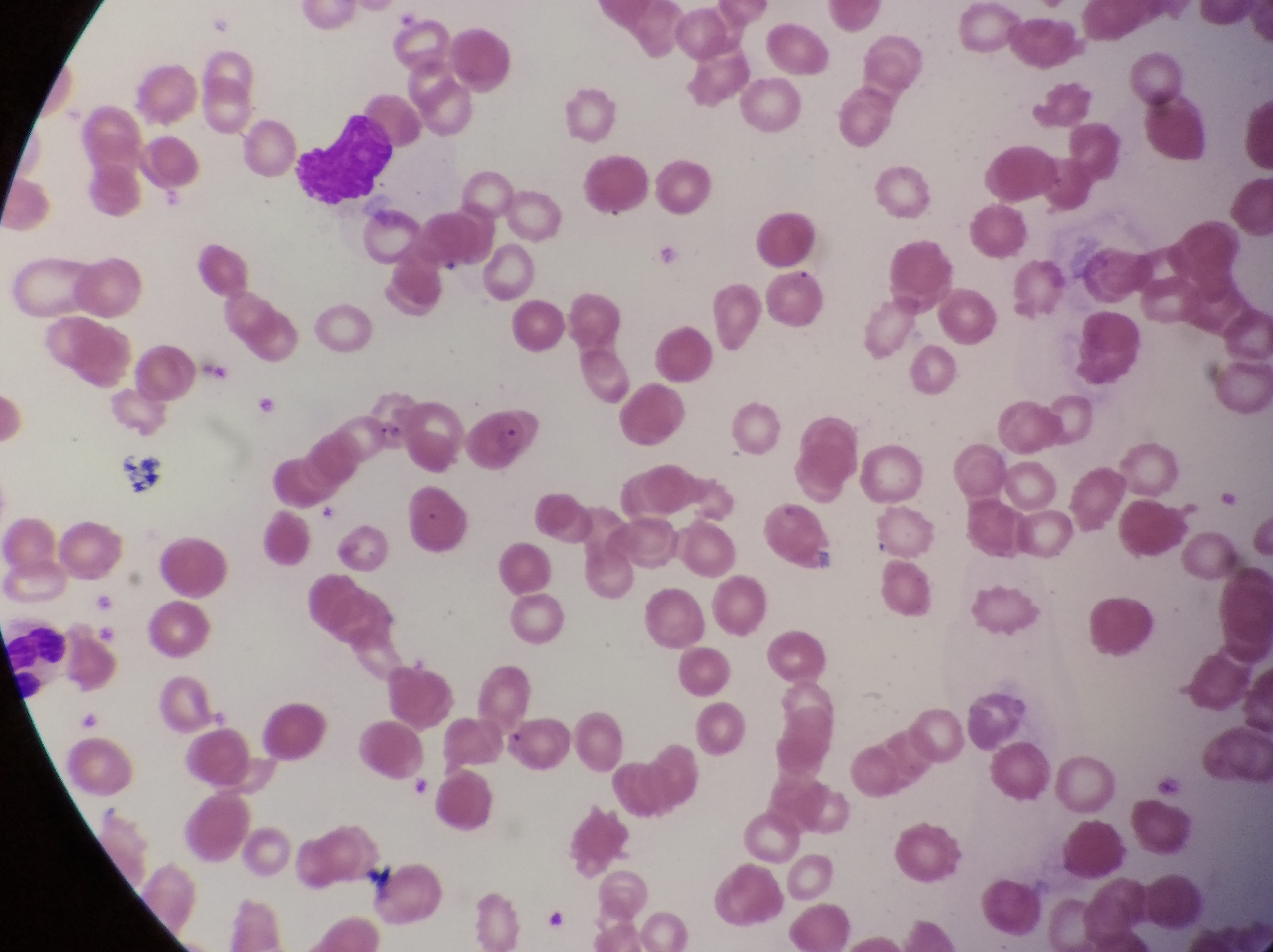
magnification = 1000x
field of view = single
leukocyte locations = approximate bounding boxes as (left, top, right, bottom) in pixels: (281, 105, 389, 204), (3, 618, 79, 698)
parasitised red blood cell locations = approximate bounding boxes as (left, top, right, bottom) in pixels: (470, 405, 544, 470)
capture = smartphone photograph through the eyepiece of an Olympus CX-23 microscope
image size = 1273×952 pixels
preparation = thin blood film
artifact (platelet-like body, stain precipitate, or debris) locations = approximate bounding boxes as (left, top, right, bottom) in pixels: (110, 452, 165, 502)
country = Uganda